Assess this cell for malaria.
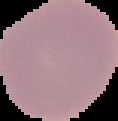
It is uninfected.

Segmented cell region on a black background. Image is 118×121 pixels. From a thin blood film.